Assess the morphology of the erythrocytes.
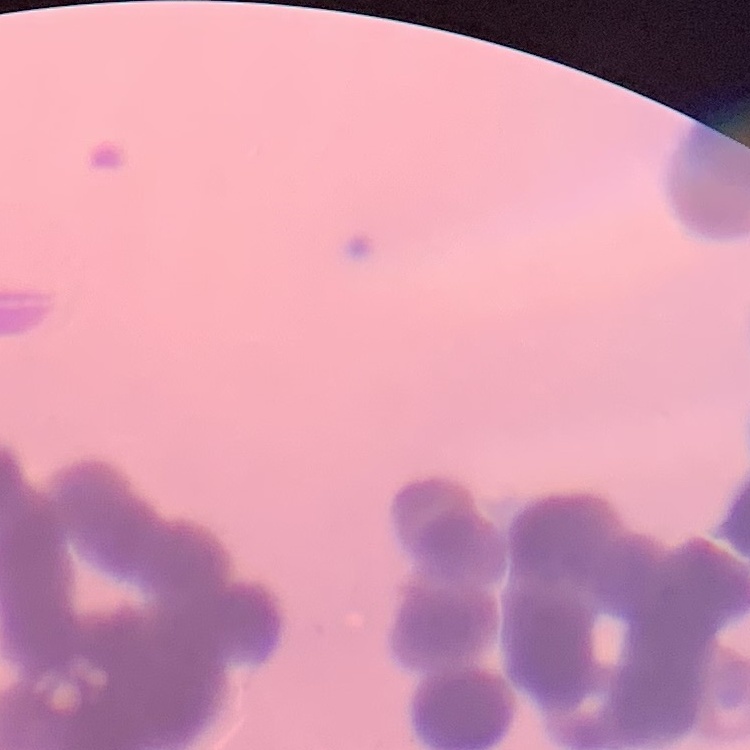
Rouleaux formation.

One tile cut from a larger photomicrograph. Field's or Giemsa stain. Thin blood film.